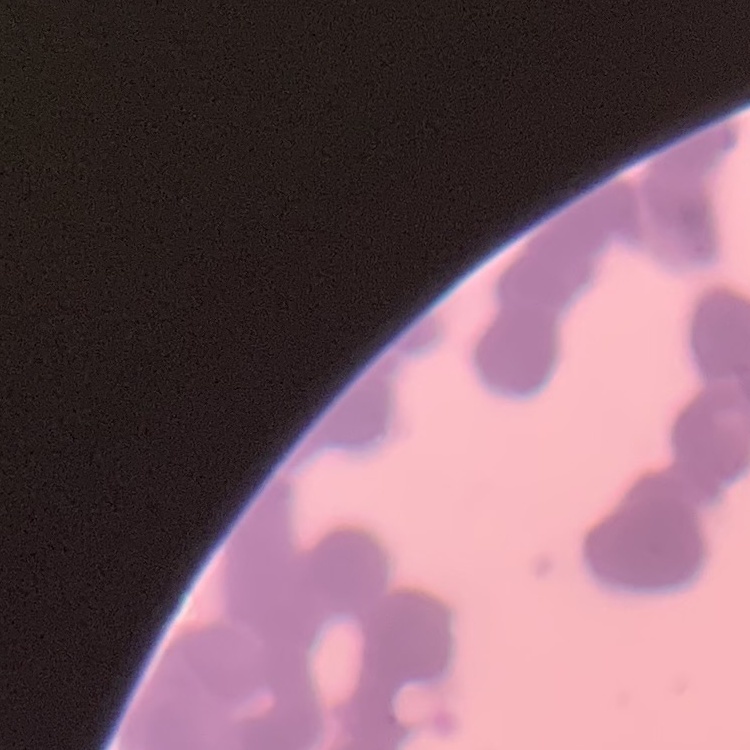
The erythrocytes exhibit rouleaux formation. Thin blood smear. Field's or Giemsa stain. Square crop of a larger photomicrograph.